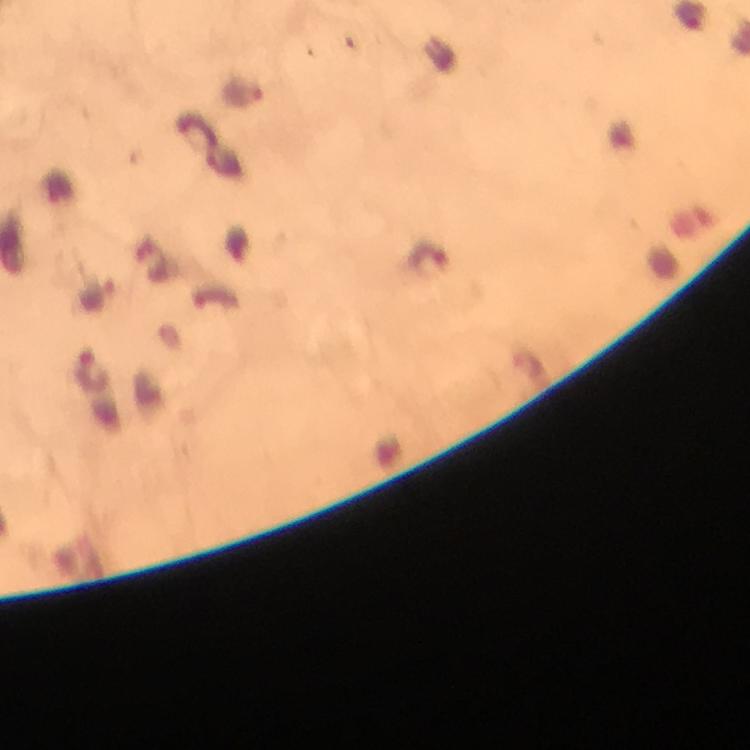
Approximate centers as (x, y) in pixels. Malaria parasite locations: (244, 92), (428, 258), (94, 372). Thick blood smear. Immersion oil applied. From a diagnostic examination for malaria. Giemsa-stained preparation. Image is 750×750 pixels. Photographed through the microscope with a smartphone camera. Cropped region of a single field of view. At 100x magnification.